Assess this cell for malaria.
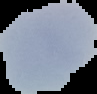
Uninfected.

The area outside the segmented cell region is set to black. From a thin blood smear. Image is 97×94 pixels.